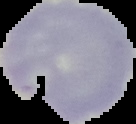

image type = cell region segmented out of the field of view; surrounding area masked to black
image size = 136×124 pixels
preparation = thin blood film
result = no Plasmodium parasites detected